Describe the morphology of the red blood cells.
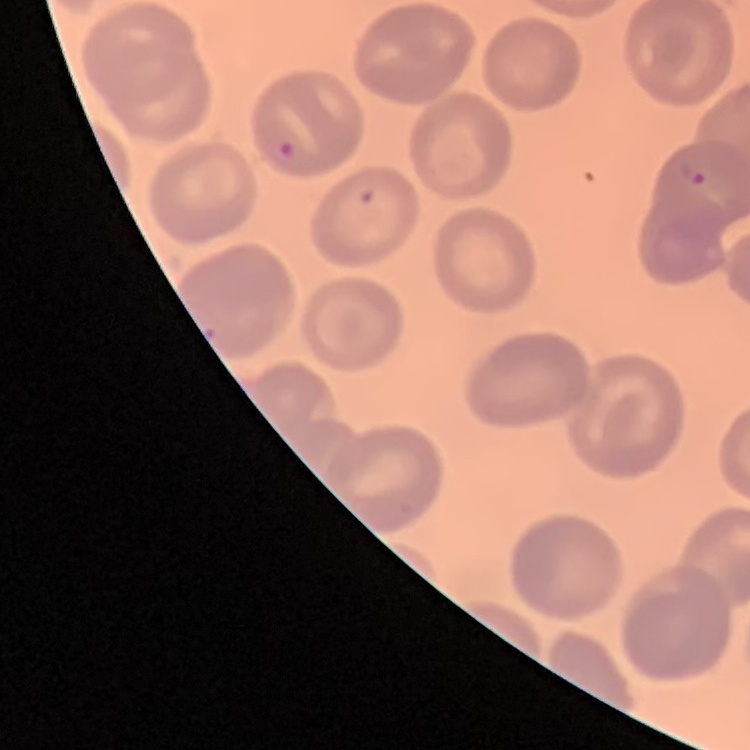

No rouleaux formation.

Summary:
  - Preparation: thin blood film
  - Image type: square crop of a larger photomicrograph
  - Stain: Field's or Giemsa